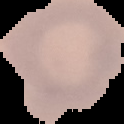

Summary:
  - Image type: cell region segmented out of the field of view; surrounding area masked to black
  - Result: negative for malaria parasites
  - Preparation: thin blood smear
  - Image size: 124×124 pixels